Locate every malaria parasite.
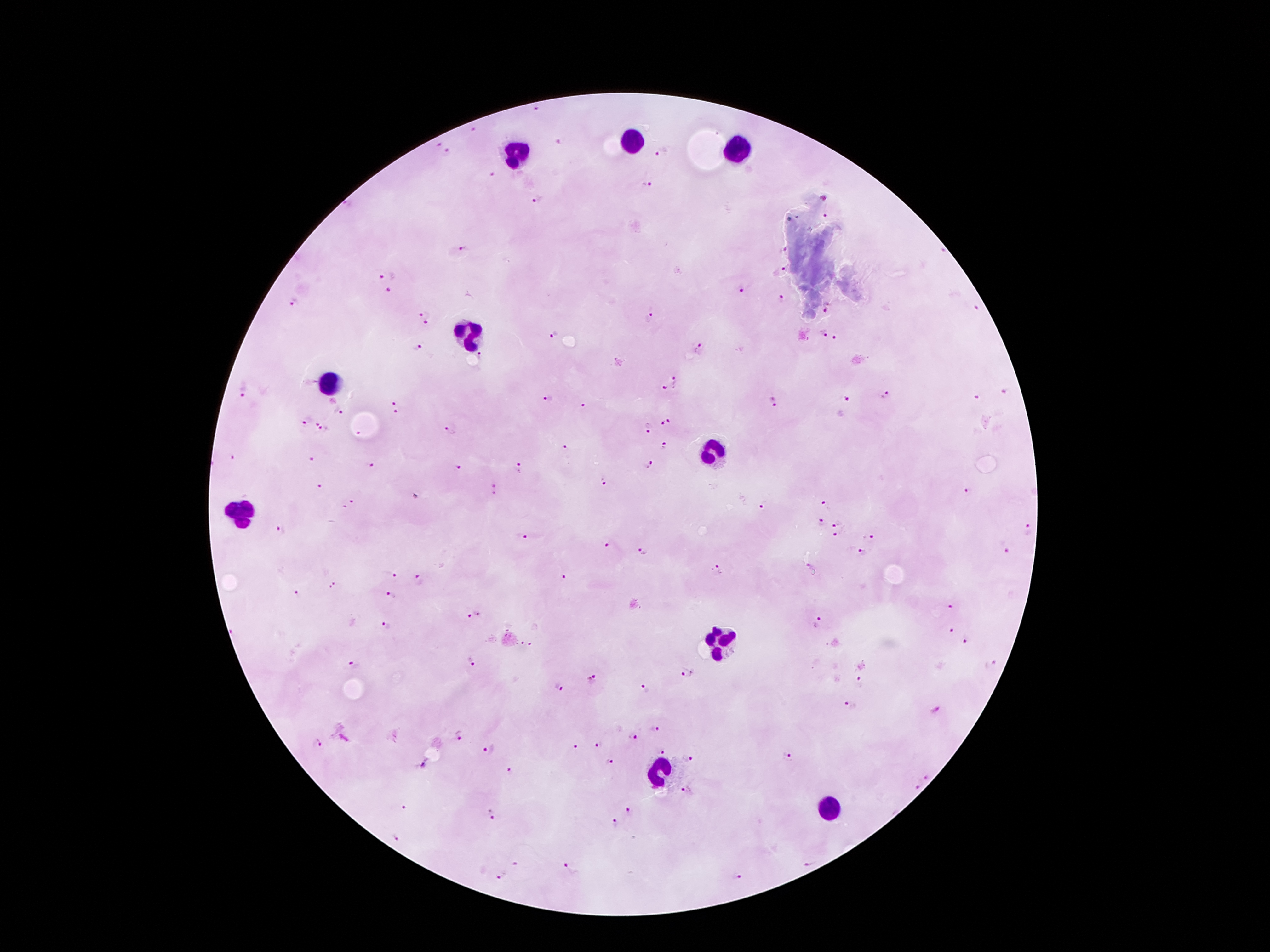
Approximate centers as [x, y] in pixels.
Malaria parasites: [537, 108], [476, 131], [561, 143], [439, 145], [661, 151], [449, 153], [496, 175], [646, 185], [538, 197], [825, 215], [466, 247], [784, 251], [781, 270], [386, 276], [743, 289], [390, 291], [782, 299], [293, 302], [978, 308], [827, 309], [424, 310], [649, 318], [425, 323], [823, 332], [555, 333], [836, 339], [418, 347], [699, 349], [482, 357], [676, 381], [666, 389], [242, 390], [1005, 392], [886, 395], [977, 398], [848, 399], [547, 400], [395, 401], [773, 402], [584, 406], [338, 411], [396, 414], [670, 421], [305, 422], [319, 422], [662, 424], [649, 428], [323, 431], [451, 432], [361, 434], [566, 447], [666, 447], [234, 457], [310, 459], [370, 465], [649, 465], [458, 468], [519, 469], [604, 481], [321, 485], [497, 488], [970, 491], [350, 504], [825, 504], [762, 507], [819, 522], [838, 523], [281, 530], [1028, 531], [837, 535], [526, 536], [871, 538], [607, 546], [1002, 547], [642, 550], [862, 552], [718, 570], [391, 575], [561, 576], [420, 580], [335, 585], [296, 594], [392, 596], [949, 606], [475, 615], [817, 620], [387, 624], [952, 630], [965, 640], [527, 646], [470, 660], [353, 664], [990, 664], [686, 674], [860, 678], [591, 679], [558, 687], [644, 689], [851, 705], [936, 709], [653, 731], [460, 735], [632, 737], [316, 743], [597, 745], [575, 746], [489, 751], [662, 752], [788, 757], [691, 760], [610, 762], [509, 771], [926, 777], [915, 787], [686, 790], [403, 807], [628, 811], [491, 814], [613, 824], [395, 836], [809, 861], [515, 864], [567, 868], [738, 875], [500, 876].

Leukocyte locations: [631, 142], [740, 148], [518, 152], [474, 332], [331, 385], [709, 455], [241, 511], [720, 644], [661, 771], [833, 808]. 100x magnification. Photographed through the microscope eyepiece with a smartphone camera. Patient malaria status: positive for Plasmodium falciparum. Image is 1270×952 pixels. One field from this slide. Thick blood smear. Giemsa-stained preparation.